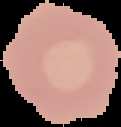

preparation = thin blood smear
image size = 121×127 pixels
result = no Plasmodium parasites seen
image type = segmented cell region on a black background